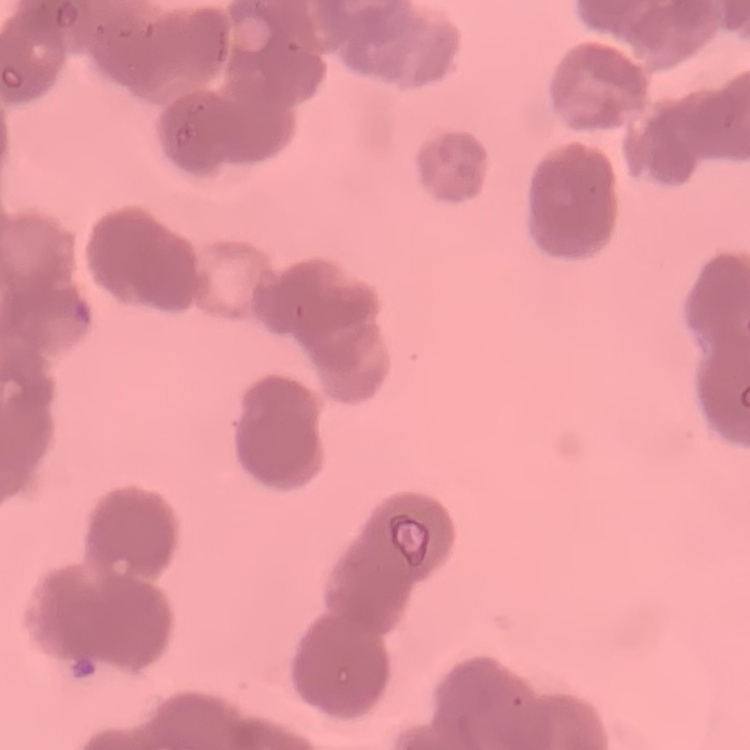 The red blood cells exhibit rouleaux formation. Thin blood film. One tile cut from a larger photomicrograph. Field's or Giemsa stain.